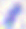

modality = photomicrograph
identification = Toxoplasma gondii
magnification = 400x